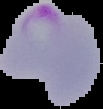

{
  "image_size": "103×109 pixels",
  "preparation": "thin blood film",
  "image_type": "segmented cell region with the area outside set to black",
  "result": "malaria parasites detected"
}